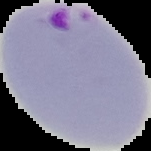
Image is 151×151 pixels. From a thin blood film. Result: Plasmodium parasites detected. The area outside the segmented cell region is set to black.